Look for Plasmodium parasites.
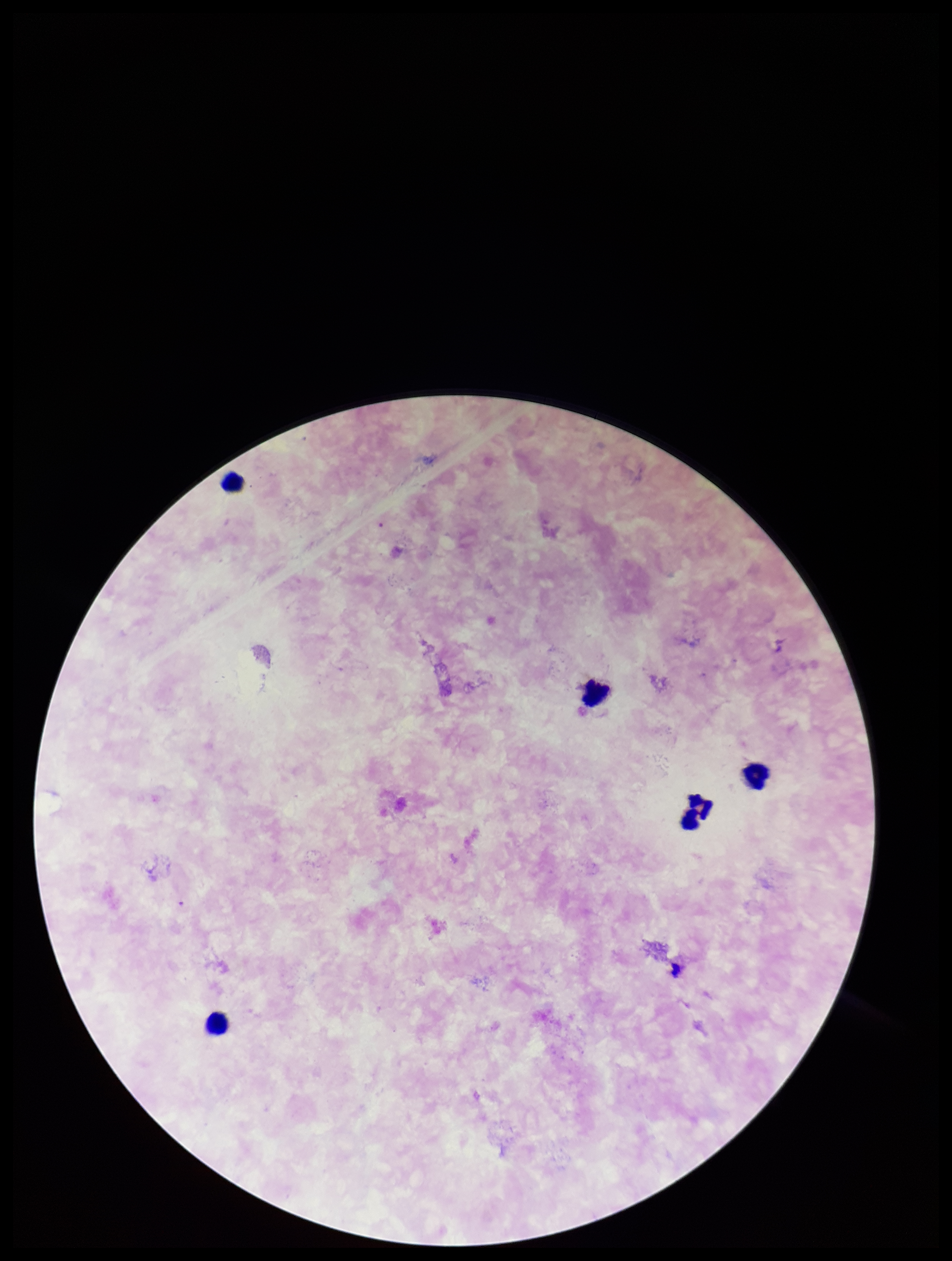

None detected.

preparation = thick smear
capture = smartphone photograph through the microscope eyepiece
stain = Giemsa
field of view = single
patient malaria status = negative
parasite count = 0
leukocyte count = 5
image size = 952×1261 pixels